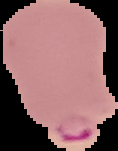
Summary:
  - Image size: 118×151 pixels
  - Preparation: thin blood film
  - Image type: cell region segmented out of the field of view; surrounding area masked to black
  - Malaria status: parasitized